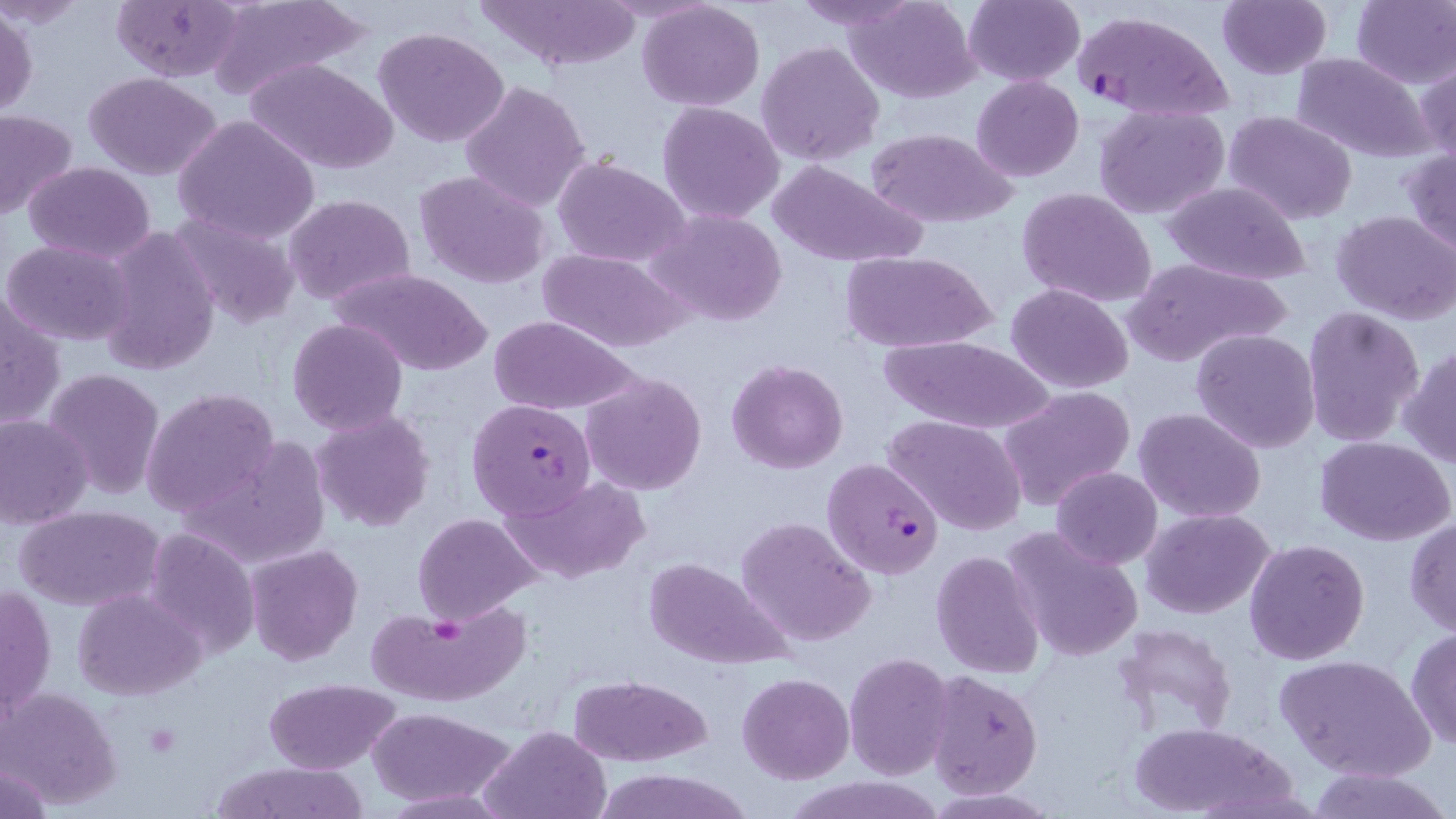
slide-level diagnosis = Plasmodium falciparum
uninfected red blood cell locations = approximate bounding boxes as [x1, y1, x2, y2] in pixels: [475, 0, 642, 72], [787, 0, 923, 31], [846, 0, 981, 102], [964, 0, 1084, 86], [1216, 0, 1332, 79], [1351, 0, 1456, 88], [112, 1, 245, 83], [205, 1, 364, 103], [636, 2, 765, 111], [1, 7, 39, 120], [374, 25, 512, 148], [756, 41, 885, 167], [1291, 53, 1433, 163], [244, 57, 397, 174], [1417, 58, 1455, 168], [83, 72, 223, 180], [971, 75, 1084, 182], [459, 79, 591, 212], [657, 101, 784, 226], [1093, 103, 1230, 220], [0, 109, 80, 219], [1226, 110, 1358, 224], [173, 114, 320, 244], [864, 127, 1018, 229], [1401, 149, 1456, 257], [553, 156, 690, 268], [23, 160, 155, 264], [768, 160, 925, 269], [413, 169, 554, 292], [1162, 181, 1313, 286], [1016, 187, 1159, 312], [284, 193, 417, 308], [647, 209, 788, 327], [1332, 209, 1456, 326], [170, 212, 302, 330], [97, 227, 220, 376], [3, 239, 135, 347], [534, 247, 688, 352], [839, 251, 997, 353], [1122, 255, 1292, 367], [334, 268, 490, 377], [1005, 284, 1134, 394], [2, 293, 65, 431], [1301, 305, 1426, 447], [488, 316, 636, 416], [287, 317, 409, 434], [1190, 328, 1322, 454], [875, 334, 1056, 435], [1400, 345, 1456, 471], [726, 358, 849, 474], [43, 368, 166, 500], [580, 371, 708, 496], [998, 386, 1136, 510], [140, 387, 280, 519], [1134, 407, 1267, 525], [310, 410, 435, 531], [0, 413, 94, 529], [884, 415, 1026, 536], [180, 434, 332, 572], [1315, 436, 1456, 546], [1050, 468, 1163, 568], [502, 474, 650, 583], [14, 504, 164, 611], [1142, 507, 1277, 619], [412, 513, 542, 625], [736, 515, 876, 647], [1404, 518, 1456, 636], [1003, 526, 1142, 663], [143, 529, 260, 659], [1243, 538, 1369, 666], [244, 543, 363, 664], [931, 551, 1043, 679], [642, 558, 791, 667], [2, 581, 56, 719], [72, 588, 205, 699], [369, 603, 528, 708], [1111, 623, 1239, 742], [1404, 628, 1456, 752], [844, 652, 954, 779], [1273, 653, 1435, 780], [925, 670, 1044, 796], [738, 673, 853, 783], [570, 674, 712, 767], [263, 678, 402, 773], [1, 686, 122, 807], [369, 707, 515, 807], [1127, 721, 1296, 818], [480, 725, 610, 818], [210, 762, 370, 819], [0, 763, 52, 818], [1302, 765, 1450, 819], [600, 771, 751, 818], [785, 777, 944, 819]
Plasmodium falciparum-infected red blood cell locations = approximate bounding boxes as [x1, y1, x2, y2] in pixels: [1072, 11, 1234, 122], [466, 398, 597, 519], [823, 455, 945, 579]
preparation = thin blood film
magnification = 1000x
field of view = one of a larger specimen
stain = May-Grünwald-Giemsa
modality = optical microscopy
image size = 1456×819 pixels